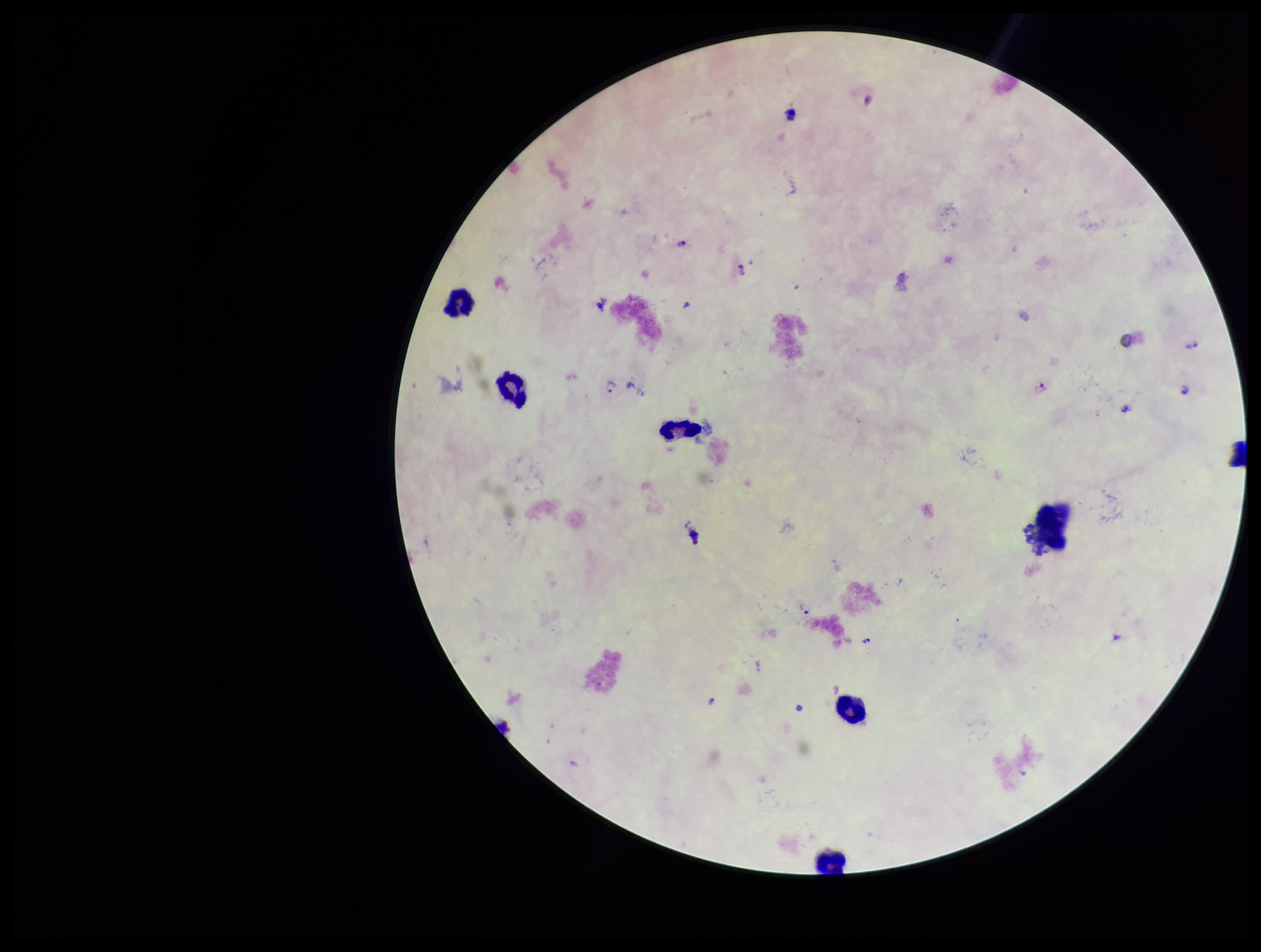

Summary:
  - Stain: Giemsa
  - Leukocyte count: 6
  - Plasmodium parasites: detected
  - Capture: smartphone photograph through the microscope eyepiece
  - Image size: 1261×952 pixels
  - Preparation: thick blood smear
  - Field of view: single
  - Species reported for this patient: Plasmodium falciparum
  - Patient malaria status: positive
  - Parasite count: 7